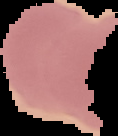

{
  "image_type": "segmented cell region on a black background",
  "preparation": "thin blood smear",
  "image_size": "118×136 pixels",
  "malaria_status": "uninfected"
}